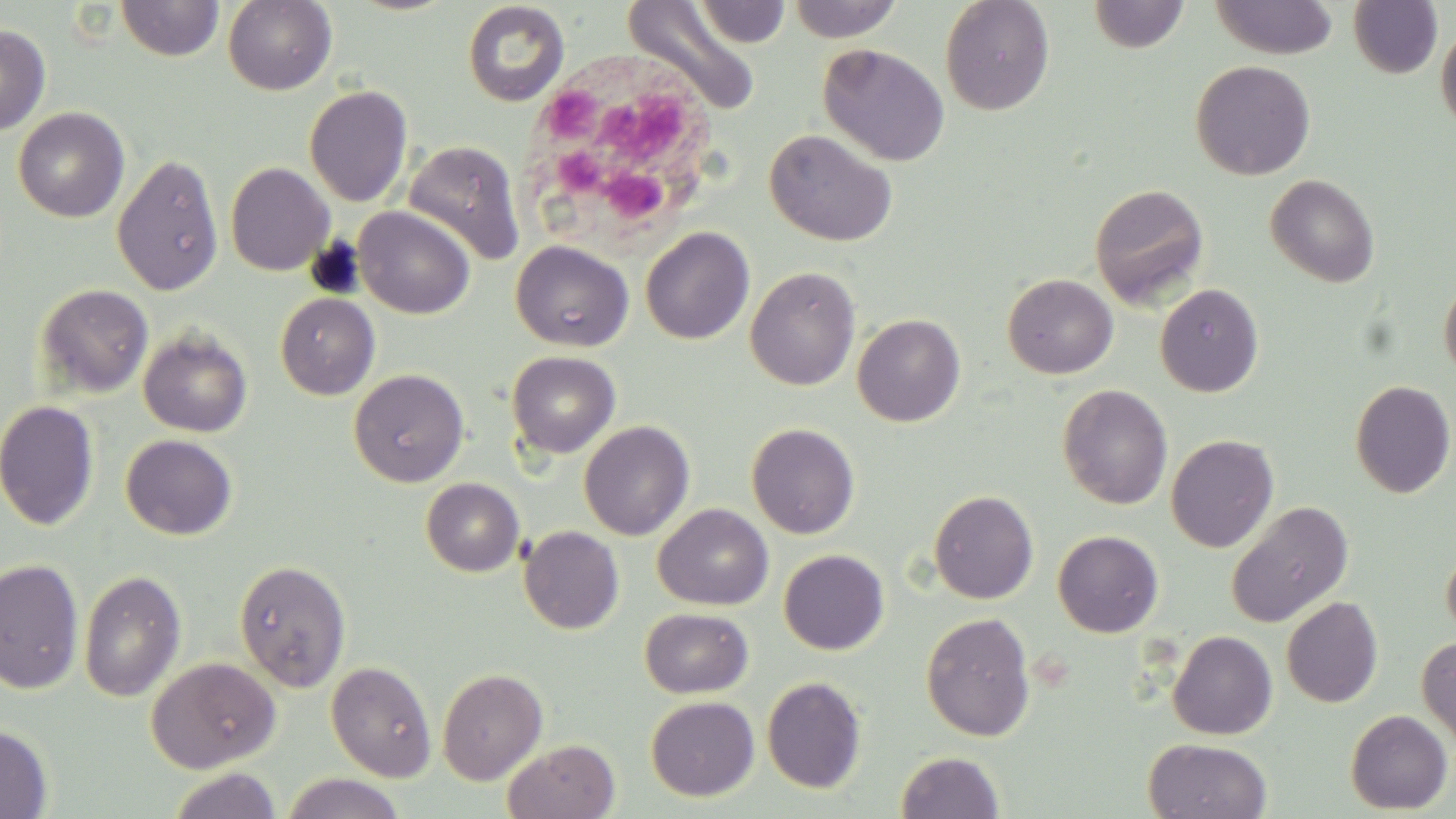
{
  "slide_level_diagnosis": "no evidence of blood parasites",
  "uninfected_red_blood_cell_locations": "approximate bounding boxes as (x1, y1, x2, y2) in pixels: (116, 0, 224, 61), (222, 0, 337, 95), (788, 0, 902, 42), (940, 0, 1055, 115), (1209, 0, 1339, 59), (1347, 0, 1443, 79), (621, 1, 763, 116), (1088, 1, 1190, 53), (461, 2, 570, 107), (693, 2, 792, 47), (1435, 22, 1456, 134), (0, 24, 50, 135), (817, 43, 950, 167), (1191, 60, 1316, 180), (304, 85, 413, 207), (12, 106, 129, 222), (764, 128, 898, 247), (403, 140, 525, 266), (112, 154, 224, 295), (225, 161, 335, 276), (1265, 173, 1380, 287), (1090, 183, 1210, 309), (353, 206, 475, 319), (640, 227, 754, 344), (510, 240, 634, 352), (745, 266, 861, 390), (1002, 273, 1118, 379), (1439, 276, 1456, 385), (34, 283, 154, 400), (1154, 283, 1264, 397), (275, 293, 379, 400), (853, 314, 965, 426), (138, 326, 253, 437), (506, 350, 620, 458), (348, 368, 469, 487), (1350, 379, 1456, 498), (1057, 383, 1173, 509), (0, 400, 100, 531), (578, 419, 695, 541), (746, 422, 860, 539), (121, 434, 237, 539), (1166, 434, 1279, 553), (420, 478, 524, 576), (928, 489, 1039, 604), (1226, 500, 1354, 628), (653, 503, 773, 610), (518, 525, 624, 634), (1052, 530, 1164, 637), (1440, 537, 1456, 645), (778, 549, 889, 655), (0, 557, 84, 694), (234, 559, 351, 691), (78, 569, 186, 702), (1281, 596, 1383, 708), (639, 607, 753, 698), (920, 612, 1036, 742), (1168, 630, 1278, 739), (1417, 635, 1456, 748), (146, 656, 282, 773), (326, 660, 437, 782), (436, 667, 548, 785), (761, 676, 867, 793), (645, 696, 759, 801), (1345, 709, 1453, 814), (0, 725, 53, 818), (1143, 737, 1272, 819), (504, 739, 620, 818), (895, 750, 1004, 818), (167, 767, 281, 819), (283, 772, 405, 819)",
  "stain": "May-Grünwald-Giemsa",
  "modality": "light microscopy",
  "preparation": "thin blood film",
  "field_of_view": "one of a larger specimen",
  "white_blood_cell_locations": "approximate bounding boxes as (x1, y1, x2, y2) in pixels: (524, 60, 728, 255)",
  "magnification": "1000x",
  "image_size": "1456×819 pixels"
}